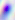
magnification: 400x
identification: Toxoplasma gondii
modality: micrograph